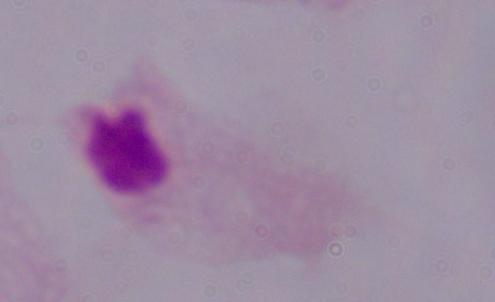
Summary:
  - Magnification: 1000x
  - Modality: photomicrograph
  - Identification: trichomonad